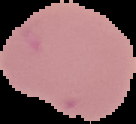

Image is 136×124 pixels. Malaria status: uninfected. From a thin blood smear. The area outside the segmented cell region is set to black.